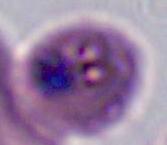 A Plasmodium parasite is shown. 400x or 1000x magnification. Photomicrograph.